Identify the blood parasite species.
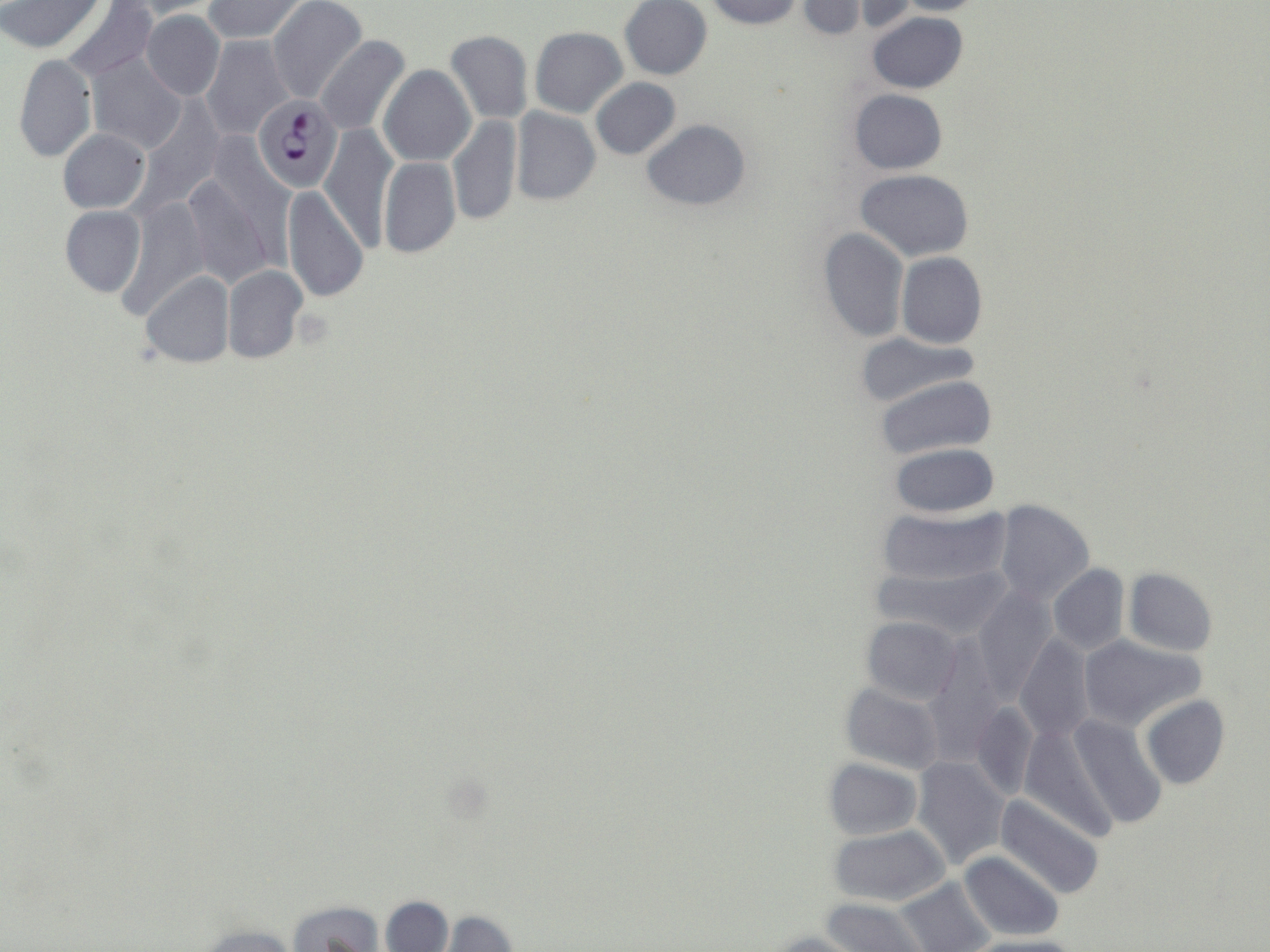
Plasmodium falciparum.

Summary:
  - Coordinate format: approximate bounding boxes as (x1,y1)-(x2,y2) corner pairs in pixels
  - Uninfected red blood cell locations: (1,0)-(104,52), (120,0)-(222,19), (203,0)-(308,43), (268,0)-(367,104), (608,0)-(702,155), (706,0)-(804,29), (795,0)-(867,39), (845,0)-(920,32), (891,0)-(992,14), (60,1)-(157,80), (619,1)-(711,80), (140,10)-(225,100), (867,12)-(967,93), (530,26)-(627,117), (445,30)-(534,126), (200,35)-(294,140), (315,36)-(409,136), (12,53)-(98,164), (86,53)-(185,154), (379,65)-(475,165), (591,79)-(681,160), (848,88)-(948,175), (135,101)-(222,210), (510,106)-(601,206), (446,116)-(521,226), (642,119)-(750,210), (320,122)-(399,252), (58,130)-(150,213), (378,158)-(460,258), (181,166)-(281,289), (855,169)-(973,262), (283,186)-(369,303), (115,194)-(209,319), (60,206)-(146,298), (817,227)-(909,343), (896,252)-(987,349), (222,265)-(306,362), (141,271)-(234,368), (852,331)-(983,407), (875,374)-(997,463), (888,443)-(1000,519), (992,499)-(1094,606), (875,506)-(1011,590), (870,561)-(1012,638), (1048,564)-(1131,654), (1124,568)-(1218,657), (972,588)-(1058,700), (861,615)-(963,704), (923,632)-(1007,751), (1014,633)-(1096,741), (1076,633)-(1207,731), (839,682)-(945,775), (1141,695)-(1230,789), (968,700)-(1038,800), (1067,713)-(1167,829), (1018,722)-(1121,841), (912,756)-(1010,868), (823,758)-(922,839), (994,794)-(1106,900), (828,826)-(951,909), (959,851)-(1064,942), (894,876)-(990,952), (379,896)-(453,951), (821,898)-(927,951), (287,899)-(385,951), (433,912)-(520,951), (190,924)-(305,952), (767,931)-(862,952), (960,936)-(1084,952)
  - Plasmodium falciparum-infected red blood cell locations: (253,95)-(341,191)
  - Stain: May-Grünwald-Giemsa
  - Preparation: thin blood film
  - Modality: optical microscopy
  - Magnification: 1000x
  - Image size: 1270×952 pixels
  - Field of view: single